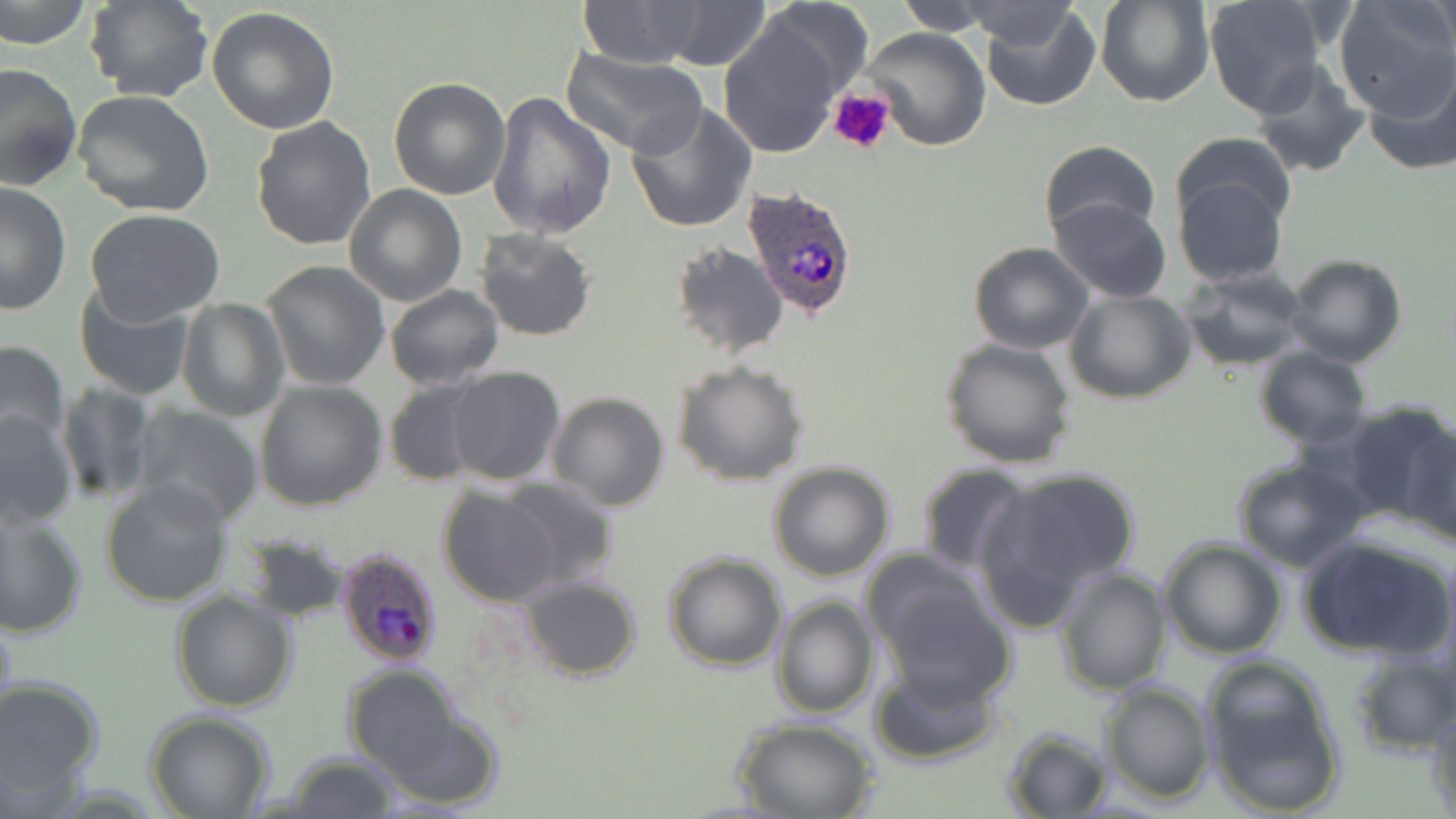 Approximate bounding boxes as (x1,y1)-(x2,y2) corner pairs in pixels. Platelet locations: (828,89)-(896,157). Uninfected red blood cell locations: (0,0)-(93,51), (86,0)-(215,104), (575,0)-(706,68), (759,0)-(875,105), (891,0)-(1005,34), (1094,0)-(1213,106), (1204,0)-(1326,117), (1436,0)-(1455,65), (959,1)-(1086,52), (978,1)-(1100,111), (1331,1)-(1456,119), (657,2)-(771,70), (207,6)-(340,134), (716,17)-(845,159), (863,27)-(992,150), (560,48)-(706,158), (1249,61)-(1373,179), (1363,61)-(1456,176), (0,63)-(82,191), (388,77)-(511,200), (72,90)-(214,217), (487,92)-(617,239), (624,101)-(756,232), (251,115)-(378,251), (1170,131)-(1298,237), (1038,140)-(1160,242), (1173,173)-(1290,287), (0,181)-(71,314), (344,184)-(468,306), (1050,197)-(1171,303), (82,210)-(227,324), (473,227)-(599,343), (670,242)-(786,358), (968,242)-(1094,353), (1283,254)-(1407,370), (259,260)-(390,391), (1181,268)-(1310,370), (73,283)-(198,401), (384,285)-(504,390), (1067,289)-(1195,404), (177,298)-(287,421), (940,337)-(1078,469), (0,339)-(70,452), (1254,347)-(1370,447), (672,359)-(809,487), (444,366)-(565,487), (383,379)-(491,486), (254,380)-(387,513), (56,381)-(155,505), (547,392)-(670,512), (1345,403)-(1454,533), (134,405)-(264,526), (0,408)-(77,529), (1403,426)-(1456,550), (1229,456)-(1372,572), (768,462)-(894,582), (915,462)-(1037,575), (988,467)-(1141,601), (496,476)-(622,594), (101,477)-(234,607), (438,488)-(563,607), (0,508)-(88,641), (1296,532)-(1454,663), (244,533)-(350,622), (1158,538)-(1287,659), (661,551)-(787,673), (864,554)-(1004,692), (1054,566)-(1173,696), (516,576)-(643,679), (170,589)-(297,713), (769,595)-(878,718), (0,605)-(19,741), (1344,649)-(1456,756), (1199,656)-(1346,816), (868,662)-(1003,767), (343,663)-(469,785), (0,676)-(105,802), (1099,680)-(1214,804), (1427,704)-(1456,818), (145,711)-(275,819), (733,717)-(880,819), (1001,727)-(1111,816), (281,753)-(402,819). Plasmodium ovale-infected red blood cell locations: (745,186)-(860,322), (334,547)-(443,669). Slide-level diagnosis: Plasmodium ovale. Light microscopy. Image is 1456×819 pixels. Thin blood smear. Single field of view. May-Grünwald-Giemsa stain. 1000x magnification.